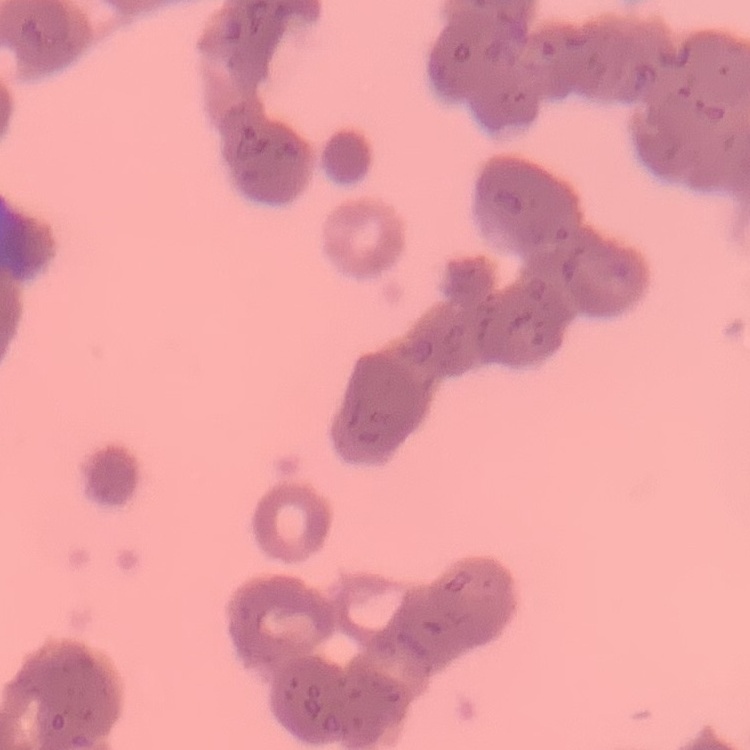
Summary:
  - Erythrocyte morphology: rouleaux formation
  - Preparation: thin blood film
  - Image type: square crop of a larger photomicrograph
  - Stain: Field's or Giemsa